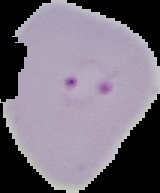

Image is 160×193 pixels. Malaria status: parasitized. Segmented cell region on a black background. From a thin blood smear.